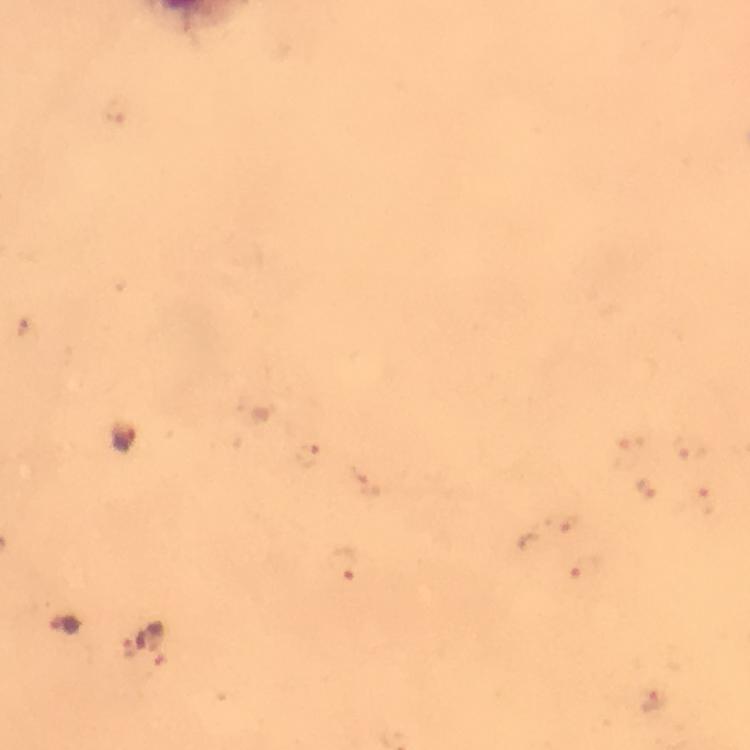

Approximate centers as {x, y} in pixels.
Summary:
  - Plasmodium parasite locations: {124, 439}, {342, 564}, {63, 626}, {129, 648}
  - Immersion oil: used
  - Preparation: thick blood smear
  - Image size: 750×750 pixels
  - Context: from a malaria diagnostic workup
  - Stain: Giemsa
  - Cropped from: one field of view
  - Capture: smartphone mounted on the microscope
  - Magnification: 100x